Identify the blood parasite species.
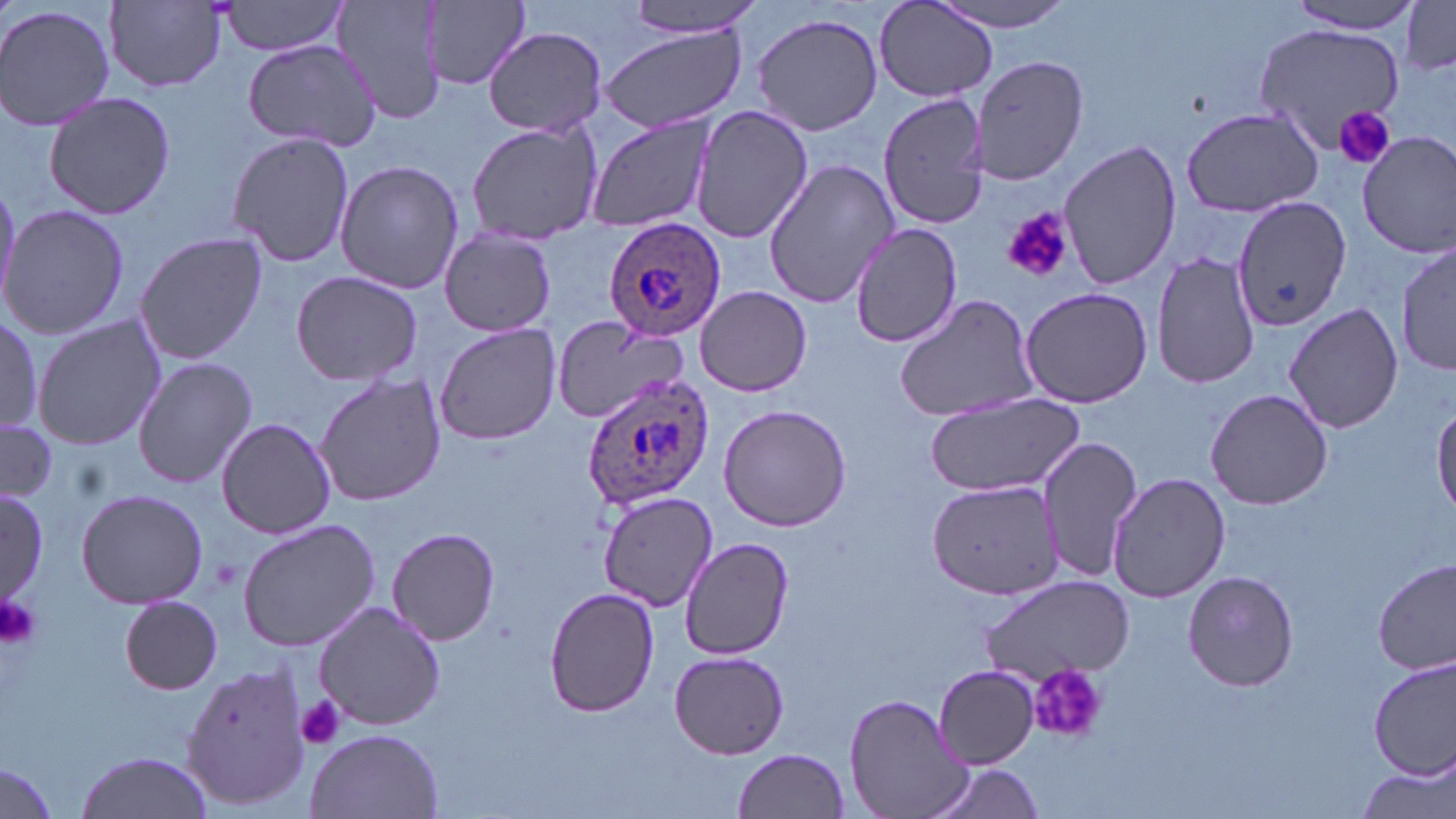

Plasmodium ovale.

Approximate bounding boxes as named x1/y1/x2/y2 corners in pixels. Plasmodium ovale-infected red blood cell locations: (x1=605, y1=216, x2=728, y2=340), (x1=579, y1=375, x2=714, y2=509). Platelet locations: (x1=1333, y1=106, x2=1397, y2=170), (x1=1000, y1=206, x2=1073, y2=284), (x1=0, y1=593, x2=43, y2=650), (x1=1028, y1=663, x2=1108, y2=744), (x1=294, y1=695, x2=347, y2=750). Uninfected red blood cell locations: (x1=218, y1=0, x2=351, y2=57), (x1=336, y1=0, x2=444, y2=125), (x1=417, y1=0, x2=536, y2=93), (x1=616, y1=0, x2=770, y2=36), (x1=930, y1=0, x2=1080, y2=34), (x1=1285, y1=0, x2=1425, y2=33), (x1=107, y1=1, x2=228, y2=91), (x1=875, y1=1, x2=996, y2=103), (x1=1398, y1=1, x2=1456, y2=74), (x1=0, y1=2, x2=118, y2=134), (x1=751, y1=11, x2=886, y2=137), (x1=1252, y1=23, x2=1405, y2=153), (x1=601, y1=25, x2=747, y2=134), (x1=483, y1=26, x2=608, y2=136), (x1=244, y1=38, x2=382, y2=152), (x1=970, y1=54, x2=1089, y2=186), (x1=40, y1=90, x2=177, y2=220), (x1=878, y1=92, x2=991, y2=232), (x1=689, y1=103, x2=812, y2=246), (x1=1181, y1=105, x2=1325, y2=217), (x1=583, y1=116, x2=716, y2=233), (x1=465, y1=121, x2=603, y2=246), (x1=227, y1=130, x2=355, y2=269), (x1=1357, y1=130, x2=1456, y2=258), (x1=1058, y1=138, x2=1181, y2=292), (x1=334, y1=160, x2=463, y2=296), (x1=762, y1=160, x2=897, y2=310), (x1=1233, y1=196, x2=1351, y2=333), (x1=0, y1=203, x2=128, y2=342), (x1=851, y1=224, x2=962, y2=347), (x1=438, y1=229, x2=555, y2=337), (x1=134, y1=232, x2=267, y2=362), (x1=1396, y1=240, x2=1454, y2=379), (x1=1152, y1=252, x2=1263, y2=391), (x1=290, y1=269, x2=423, y2=386), (x1=695, y1=285, x2=812, y2=397), (x1=1020, y1=285, x2=1153, y2=408), (x1=894, y1=294, x2=1040, y2=423), (x1=1281, y1=301, x2=1403, y2=432), (x1=0, y1=316, x2=42, y2=434), (x1=32, y1=316, x2=166, y2=451), (x1=548, y1=318, x2=689, y2=424), (x1=434, y1=322, x2=561, y2=446), (x1=132, y1=356, x2=258, y2=489), (x1=313, y1=373, x2=446, y2=506), (x1=1205, y1=387, x2=1333, y2=511), (x1=925, y1=392, x2=1085, y2=499), (x1=1432, y1=402, x2=1456, y2=517), (x1=719, y1=403, x2=852, y2=533), (x1=0, y1=415, x2=58, y2=504), (x1=215, y1=417, x2=336, y2=537), (x1=1036, y1=432, x2=1143, y2=587), (x1=1108, y1=472, x2=1232, y2=603), (x1=925, y1=479, x2=1063, y2=602), (x1=74, y1=487, x2=209, y2=608), (x1=1, y1=489, x2=48, y2=605), (x1=599, y1=492, x2=716, y2=611), (x1=236, y1=518, x2=380, y2=652), (x1=386, y1=525, x2=501, y2=645), (x1=679, y1=534, x2=794, y2=659), (x1=1374, y1=559, x2=1455, y2=677), (x1=1182, y1=569, x2=1301, y2=692), (x1=980, y1=576, x2=1134, y2=683), (x1=543, y1=586, x2=660, y2=719), (x1=119, y1=596, x2=222, y2=695), (x1=314, y1=600, x2=446, y2=730), (x1=668, y1=649, x2=791, y2=760), (x1=1369, y1=656, x2=1454, y2=783), (x1=180, y1=661, x2=311, y2=812), (x1=933, y1=665, x2=1040, y2=768), (x1=844, y1=693, x2=974, y2=819), (x1=303, y1=728, x2=444, y2=819), (x1=733, y1=749, x2=851, y2=819), (x1=72, y1=750, x2=216, y2=819), (x1=1354, y1=760, x2=1455, y2=819), (x1=0, y1=762, x2=59, y2=819), (x1=921, y1=763, x2=1048, y2=819). May-Grünwald-Giemsa stain. Thin blood smear. Light microscopy. Image is 1456×819 pixels. Single field of view. 1000x magnification.